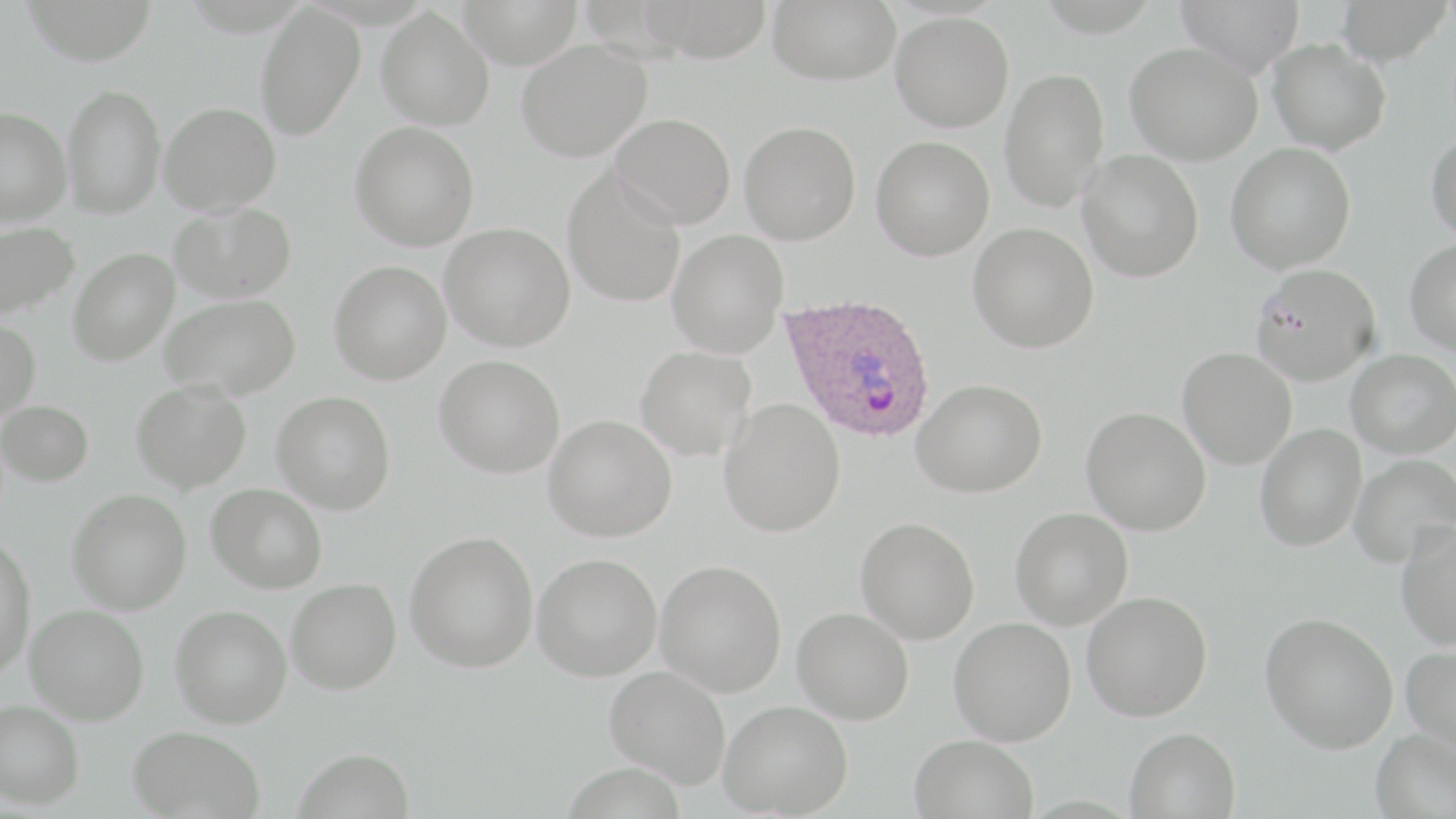
Approximate bounding boxes as (x1,y1)-(x2,y2) corner pairs in pixels. Plasmodium ovale-infected red blood cell locations: (779,292)-(937,443). Uninfected red blood cell locations: (21,0)-(158,65), (635,0)-(775,63), (768,0)-(900,85), (1175,0)-(1305,76), (1336,0)-(1451,66), (457,1)-(583,68), (255,4)-(364,140), (376,7)-(495,130), (890,11)-(1014,132), (516,38)-(652,162), (1268,39)-(1390,155), (1125,42)-(1262,165), (1000,67)-(1110,214), (62,83)-(165,218), (158,102)-(281,215), (0,107)-(72,227), (610,112)-(736,229), (739,120)-(861,244), (350,121)-(479,250), (1426,132)-(1456,243), (871,135)-(995,260), (1225,142)-(1356,273), (1077,149)-(1204,282), (562,167)-(687,308), (169,201)-(297,303), (0,221)-(79,322), (440,222)-(575,351), (968,222)-(1098,353), (667,228)-(788,358), (1405,240)-(1456,354), (68,248)-(179,366), (329,260)-(451,384), (1250,262)-(1381,384), (160,294)-(300,400), (0,319)-(40,421), (635,345)-(757,461), (1178,347)-(1297,469), (1346,348)-(1456,457), (434,354)-(565,478), (913,378)-(1046,497), (131,380)-(251,492), (272,392)-(396,513), (0,399)-(94,486), (718,399)-(845,537), (1082,406)-(1211,535), (543,415)-(677,541), (1255,424)-(1366,551), (1349,453)-(1456,568), (207,483)-(327,593), (67,489)-(191,614), (1010,507)-(1133,629), (856,516)-(979,644), (1396,521)-(1456,650), (405,530)-(538,673), (0,535)-(37,677), (532,552)-(662,681), (656,560)-(786,697), (286,578)-(401,694), (1082,591)-(1212,721), (25,604)-(150,725), (171,604)-(292,728), (793,607)-(914,724), (1260,612)-(1398,754), (949,617)-(1076,745), (1401,643)-(1456,758), (605,665)-(731,788), (0,699)-(84,809), (719,700)-(853,817), (128,725)-(266,819), (1124,727)-(1241,818), (1370,728)-(1456,819), (909,734)-(1039,819), (292,746)-(416,819). Slide-level diagnosis: Plasmodium ovale. May-Grünwald-Giemsa stain. 1000x magnification. Image is 1456×819 pixels. Thin blood smear. Optical microscopy. Single field of view.